Classify this cell by malaria status.
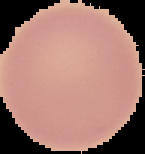

It is uninfected.

image type = segmented cell region on a black background
preparation = thin blood film
image size = 145×154 pixels